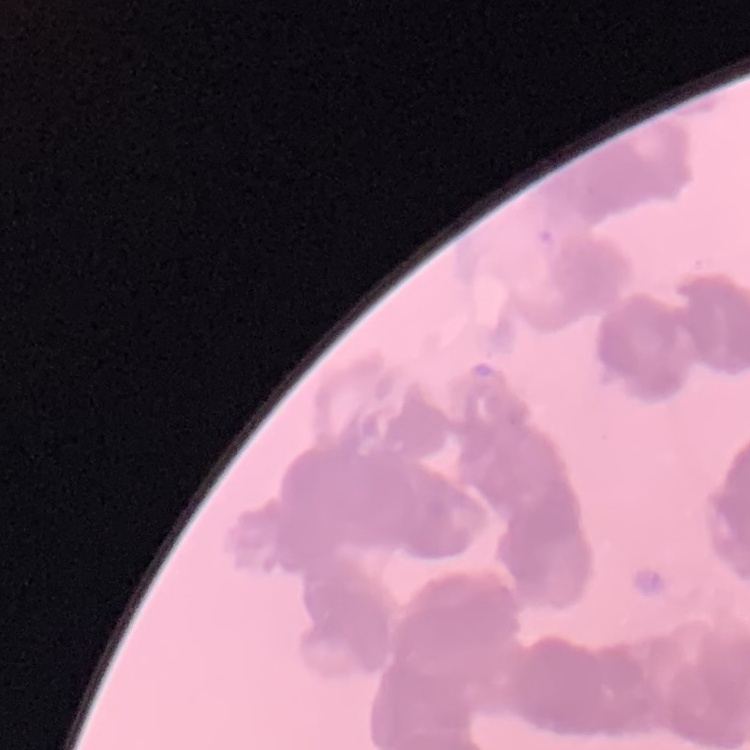
erythrocyte morphology = rouleaux formation
preparation = thin blood smear
stain = Field's or Giemsa
image type = square crop of a larger photomicrograph